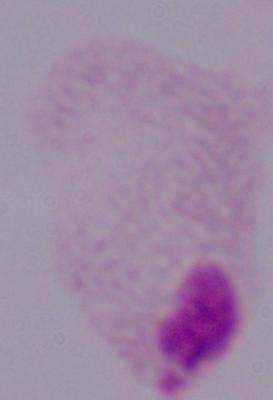
modality = micrograph
magnification = 1000x
identification = trichomonad